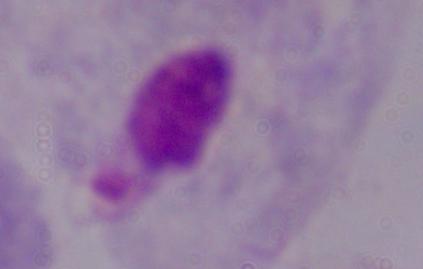

magnification: 1000x
modality: photomicrograph
identification: trichomonad